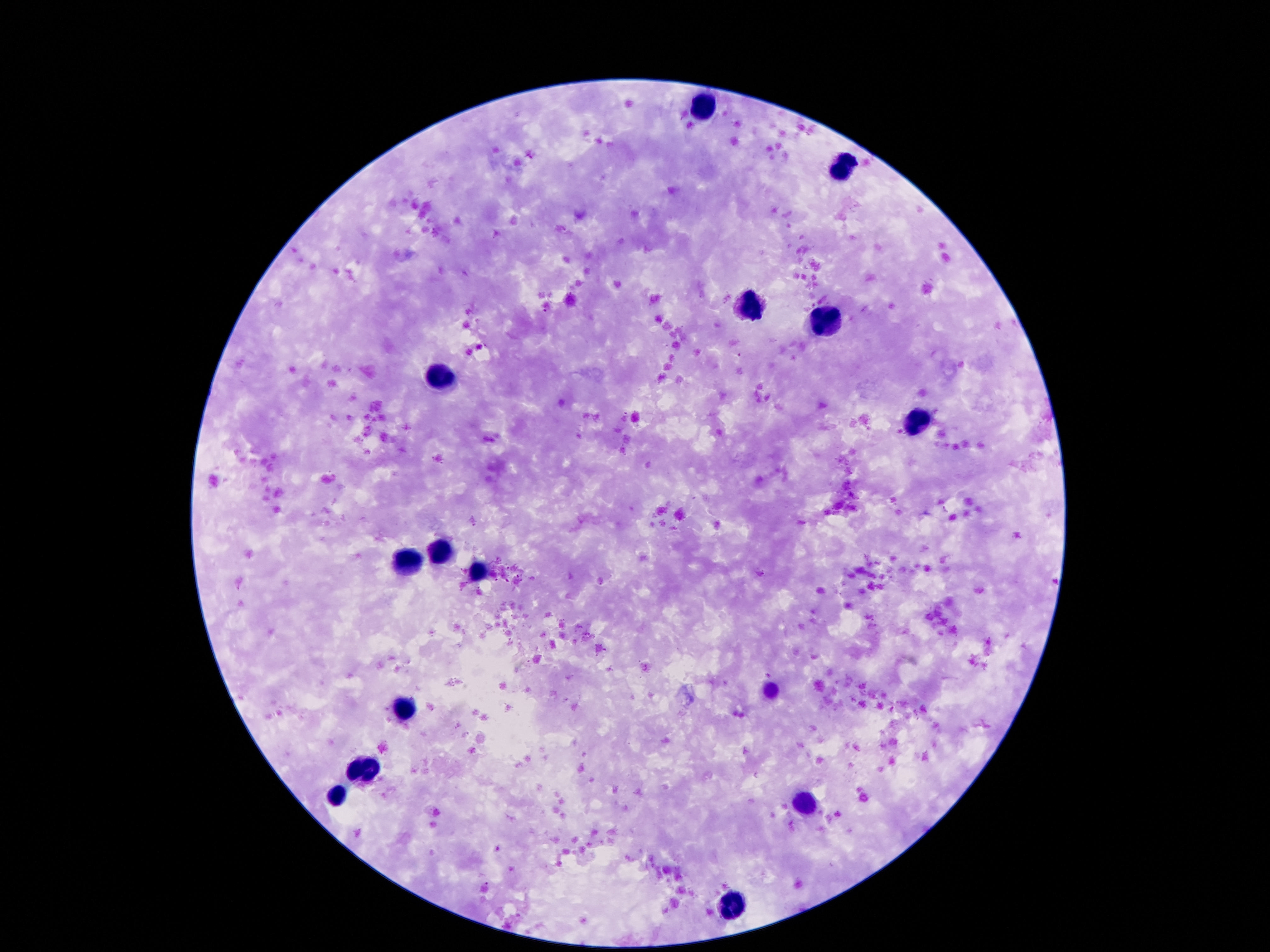

Approximate centers as {x, y} in pixels. Leukocyte locations: {702, 112}, {839, 167}, {749, 302}, {822, 320}, {440, 376}, {917, 419}, {440, 552}, {409, 561}, {480, 572}, {403, 712}, {362, 774}, {335, 800}, {804, 806}, {734, 904}. Smartphone photograph taken through the microscope eyepiece. Thick blood film. One field from this slide. 100x magnification. Patient malaria status: uninfected. Giemsa stain. Image is 1270×952 pixels.